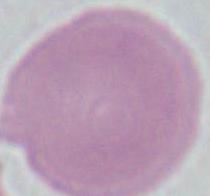

identification = erythrocyte
modality = photomicrograph
magnification = 1000x